Name the parasite shown.
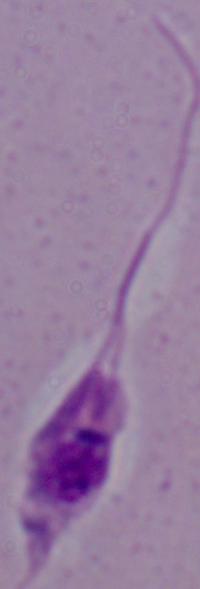
This is Leishmania.

Captured at 1000x magnification. Micrograph.